Locate every cell, classifying each as a parasitized red blood cell, an uninfected red blood cell, or a white blood cell.
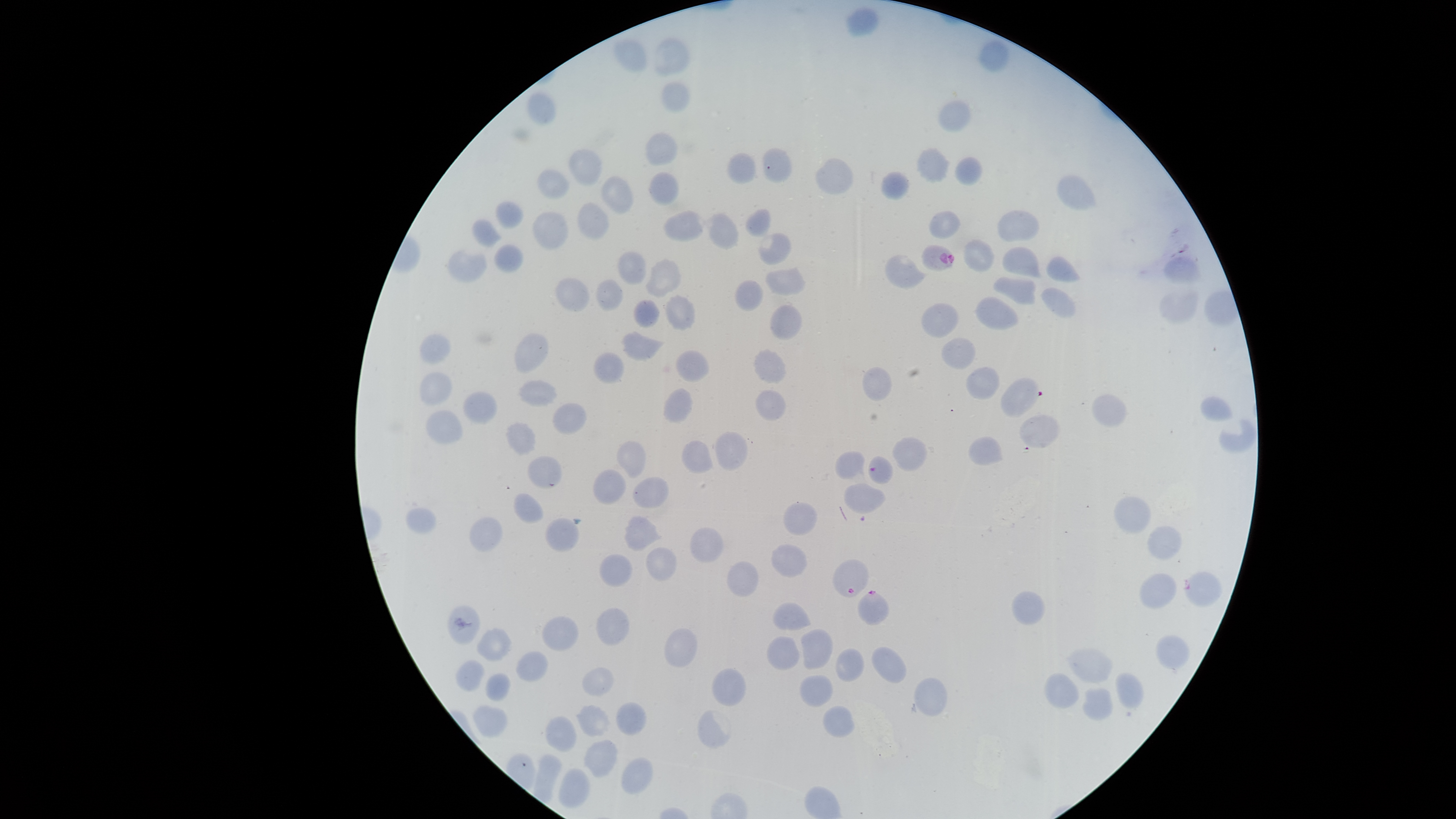

Approximate bounding boxes, in pixels from the top-left corner.
Parasitized red blood cells: (left=921, top=244, right=955, bottom=272), (left=868, top=455, right=893, bottom=483), (left=832, top=559, right=869, bottom=597), (left=1183, top=571, right=1222, bottom=606), (left=857, top=590, right=890, bottom=625).
Uninfected red blood cells: (left=845, top=6, right=880, bottom=36), (left=613, top=37, right=648, bottom=73), (left=650, top=37, right=690, bottom=77), (left=978, top=39, right=1010, bottom=72), (left=661, top=80, right=691, bottom=112), (left=526, top=91, right=556, bottom=125), (left=937, top=99, right=973, bottom=132), (left=644, top=131, right=679, bottom=167), (left=568, top=147, right=602, bottom=187), (left=916, top=147, right=951, bottom=183), (left=726, top=152, right=756, bottom=184), (left=954, top=156, right=983, bottom=185), (left=814, top=157, right=854, bottom=195), (left=536, top=167, right=570, bottom=198), (left=881, top=170, right=911, bottom=200), (left=648, top=171, right=679, bottom=206), (left=600, top=175, right=635, bottom=213), (left=1056, top=175, right=1097, bottom=211), (left=495, top=201, right=524, bottom=228), (left=576, top=201, right=610, bottom=240), (left=744, top=208, right=772, bottom=238), (left=532, top=210, right=569, bottom=250), (left=663, top=210, right=704, bottom=242), (left=929, top=210, right=962, bottom=240), (left=997, top=210, right=1040, bottom=243), (left=703, top=213, right=740, bottom=250), (left=471, top=219, right=502, bottom=248), (left=758, top=233, right=793, bottom=265), (left=963, top=238, right=994, bottom=272), (left=492, top=243, right=523, bottom=273), (left=1001, top=245, right=1043, bottom=278), (left=448, top=249, right=488, bottom=282), (left=616, top=250, right=647, bottom=286), (left=1045, top=254, right=1081, bottom=282), (left=885, top=255, right=929, bottom=290), (left=1162, top=255, right=1204, bottom=284), (left=644, top=257, right=682, bottom=299), (left=765, top=266, right=806, bottom=297), (left=555, top=276, right=591, bottom=312), (left=992, top=276, right=1037, bottom=306), (left=595, top=279, right=625, bottom=312), (left=735, top=279, right=764, bottom=312), (left=1041, top=287, right=1077, bottom=319), (left=1159, top=290, right=1200, bottom=324), (left=664, top=293, right=696, bottom=331), (left=975, top=295, right=1018, bottom=330), (left=633, top=299, right=661, bottom=329), (left=921, top=302, right=960, bottom=338), (left=769, top=304, right=803, bottom=341), (left=620, top=331, right=666, bottom=362), (left=514, top=333, right=549, bottom=374), (left=419, top=334, right=451, bottom=364), (left=939, top=336, right=976, bottom=370), (left=753, top=348, right=787, bottom=385), (left=676, top=349, right=709, bottom=382), (left=593, top=352, right=625, bottom=385), (left=862, top=366, right=893, bottom=401), (left=966, top=367, right=1001, bottom=401), (left=419, top=371, right=453, bottom=407), (left=517, top=379, right=558, bottom=407), (left=662, top=387, right=693, bottom=424), (left=754, top=389, right=786, bottom=422), (left=463, top=390, right=499, bottom=424), (left=1092, top=394, right=1127, bottom=427), (left=1199, top=395, right=1233, bottom=422), (left=552, top=402, right=587, bottom=436), (left=425, top=409, right=464, bottom=444), (left=1019, top=414, right=1060, bottom=448), (left=1219, top=419, right=1255, bottom=452), (left=505, top=422, right=536, bottom=456), (left=714, top=431, right=748, bottom=472), (left=892, top=436, right=928, bottom=472), (left=967, top=437, right=1005, bottom=466), (left=616, top=440, right=646, bottom=478), (left=681, top=440, right=713, bottom=474), (left=835, top=450, right=865, bottom=479), (left=527, top=455, right=562, bottom=489), (left=592, top=469, right=626, bottom=504), (left=632, top=477, right=669, bottom=508), (left=843, top=483, right=886, bottom=514), (left=513, top=493, right=544, bottom=524), (left=1113, top=495, right=1152, bottom=534), (left=783, top=502, right=818, bottom=536), (left=405, top=506, right=438, bottom=534), (left=623, top=515, right=663, bottom=552), (left=469, top=516, right=503, bottom=552), (left=544, top=516, right=580, bottom=553), (left=688, top=525, right=724, bottom=562), (left=1146, top=526, right=1182, bottom=560), (left=770, top=543, right=807, bottom=577), (left=645, top=547, right=678, bottom=581), (left=599, top=553, right=633, bottom=586), (left=726, top=561, right=759, bottom=597), (left=1139, top=573, right=1177, bottom=609), (left=1011, top=591, right=1045, bottom=625), (left=772, top=601, right=811, bottom=631), (left=447, top=604, right=481, bottom=645), (left=595, top=607, right=629, bottom=645), (left=540, top=616, right=579, bottom=652), (left=476, top=627, right=512, bottom=662), (left=665, top=628, right=698, bottom=668), (left=800, top=628, right=833, bottom=670), (left=1156, top=634, right=1190, bottom=670), (left=766, top=636, right=800, bottom=670), (left=871, top=646, right=906, bottom=683), (left=835, top=647, right=864, bottom=682), (left=1066, top=647, right=1113, bottom=685), (left=516, top=650, right=548, bottom=682), (left=455, top=661, right=485, bottom=692), (left=581, top=666, right=615, bottom=696), (left=711, top=668, right=747, bottom=706), (left=1114, top=671, right=1144, bottom=709), (left=484, top=672, right=512, bottom=701), (left=1043, top=673, right=1080, bottom=708), (left=798, top=674, right=833, bottom=708), (left=913, top=677, right=948, bottom=717), (left=1082, top=686, right=1113, bottom=722), (left=615, top=701, right=648, bottom=736), (left=576, top=705, right=610, bottom=738), (left=823, top=705, right=855, bottom=738), (left=473, top=706, right=508, bottom=739), (left=696, top=710, right=730, bottom=747), (left=544, top=716, right=578, bottom=753), (left=583, top=739, right=617, bottom=778), (left=533, top=754, right=562, bottom=804), (left=621, top=757, right=653, bottom=794), (left=558, top=767, right=590, bottom=809).
No white blood cells identified.

image_size: 1456×819 pixels
stain: Giemsa
capture: smartphone photograph through the microscope eyepiece
visible_region: circular
preparation: thin blood smear
field_of_view: single
species: Plasmodium falciparum